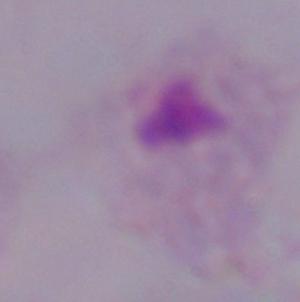
A trichomonad is seen. 1000x magnification. Micrograph.